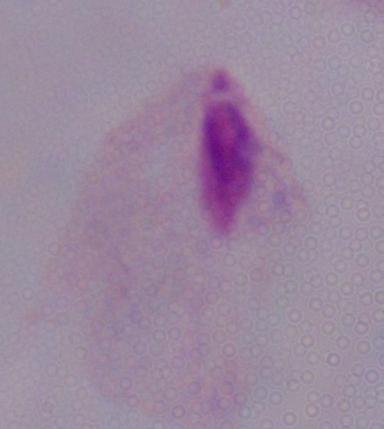
A trichomonad is seen. Photomicrograph. Captured at 1000x magnification.